Report the malaria status of this cell.
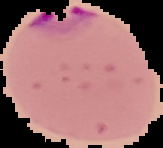

Parasitized.

From a thin blood film. Segmented cell region on a black background. Image is 163×148 pixels.